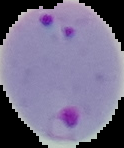
preparation = thin blood film
image size = 124×148 pixels
malaria status = parasitized
image type = segmented cell region on a black background